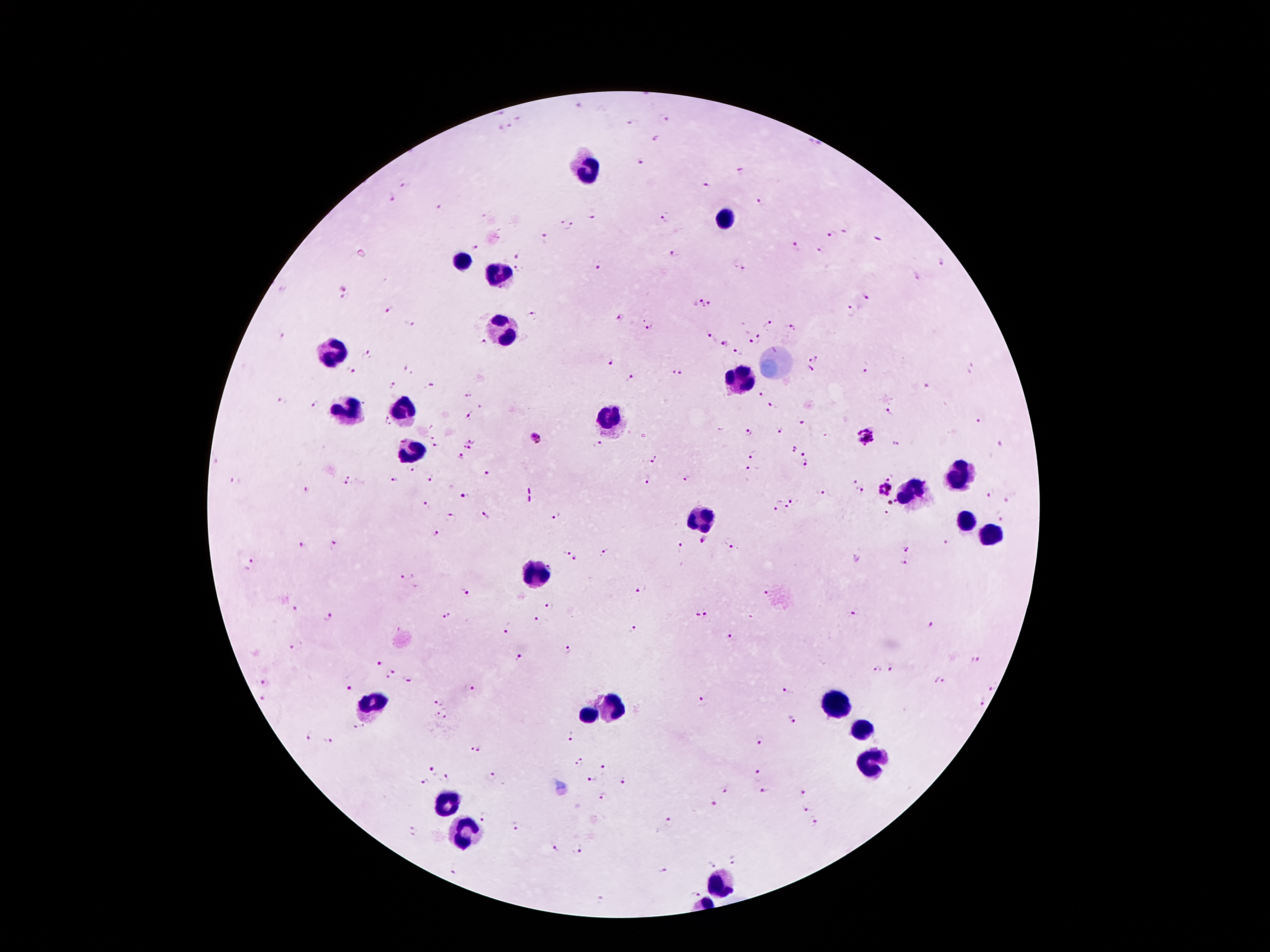

Approximate centers as [x, y] in pixels. Plasmodium parasite locations: [580, 107], [517, 118], [668, 119], [631, 124], [510, 126], [499, 127], [657, 139], [815, 144], [638, 162], [742, 170], [406, 184], [706, 186], [390, 197], [763, 202], [438, 206], [591, 215], [667, 218], [561, 221], [574, 226], [846, 228], [833, 235], [877, 238], [546, 239], [476, 246], [794, 248], [821, 249], [519, 253], [673, 254], [942, 261], [740, 267], [599, 268], [518, 269], [346, 288], [867, 295], [342, 297], [696, 299], [709, 306], [851, 309], [388, 311], [531, 314], [620, 319], [767, 322], [408, 323], [648, 323], [792, 328], [709, 336], [282, 337], [747, 338], [760, 339], [723, 344], [740, 353], [367, 354], [815, 358], [612, 361], [809, 368], [971, 368], [865, 369], [350, 371], [408, 371], [676, 372], [631, 378], [927, 385], [394, 386], [430, 386], [765, 392], [468, 394], [283, 400], [315, 404], [775, 406], [889, 413], [470, 415], [981, 419], [388, 421], [802, 423], [780, 430], [749, 432], [535, 437], [867, 437], [474, 439], [599, 444], [897, 444], [1001, 444], [437, 446], [466, 446], [792, 449], [754, 454], [804, 455], [461, 456], [654, 457], [806, 466], [412, 468], [753, 468], [488, 474], [395, 477], [432, 477], [684, 478], [890, 478], [647, 479], [234, 480], [348, 480], [853, 480], [307, 489], [885, 489], [820, 492], [862, 492], [990, 494], [465, 497], [1007, 500], [792, 501], [892, 501], [776, 503], [427, 505], [786, 508], [886, 513], [486, 515], [556, 515], [1002, 516], [452, 517], [433, 534], [704, 539], [947, 541], [731, 542], [334, 544], [302, 545], [681, 546], [906, 549], [568, 551], [604, 551], [576, 560], [250, 562], [904, 564], [408, 574], [642, 590], [464, 591], [767, 594], [551, 606], [294, 609], [696, 613], [854, 613], [448, 615], [329, 616], [707, 616], [538, 621], [931, 626], [632, 629], [506, 630], [733, 638], [295, 645], [567, 649], [521, 657], [973, 659], [378, 663], [892, 669], [876, 670], [390, 674], [406, 678], [265, 681], [938, 681], [349, 686], [992, 687], [473, 689], [787, 691], [263, 697], [440, 701], [703, 702], [984, 702], [442, 714], [793, 720], [358, 727], [573, 736], [308, 737], [762, 741], [327, 742], [477, 748], [579, 762], [602, 768], [432, 769], [759, 775], [492, 777], [446, 779], [593, 779], [624, 781], [425, 782], [725, 791], [763, 793], [804, 793], [605, 796], [715, 802], [806, 809], [484, 818], [814, 821], [669, 823], [516, 825], [414, 831], [553, 848], [578, 851], [732, 861], [711, 866], [454, 868], [663, 869], [695, 893], [601, 901]. Leukocyte locations: [590, 169], [729, 218], [460, 260], [500, 276], [503, 331], [330, 356], [737, 382], [402, 412], [348, 413], [613, 418], [412, 451], [956, 476], [913, 491], [701, 520], [966, 524], [989, 537], [533, 575], [837, 706], [373, 707], [608, 707], [585, 715], [864, 729], [869, 764], [720, 884]. Image is 1270×952 pixels. Patient malaria status: infected with Plasmodium falciparum. Thick peripheral-blood smear. 100x magnification. Giemsa stain. Single field of view. Photographed through the microscope eyepiece with a smartphone camera.